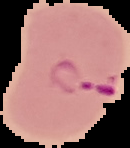

Segmented cell region on a black background. From a thin blood smear. Image is 130×148 pixels. Result: Plasmodium parasites detected.